Report the malaria status of this cell.
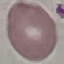

It is uninfected.

image_type: automatically extracted cell patch, resized to 64 × 64 pixels
capture: smartphone camera at the microscope eyepiece
stain: Giemsa
preparation: thin smear